Describe the morphology of the red blood cells.
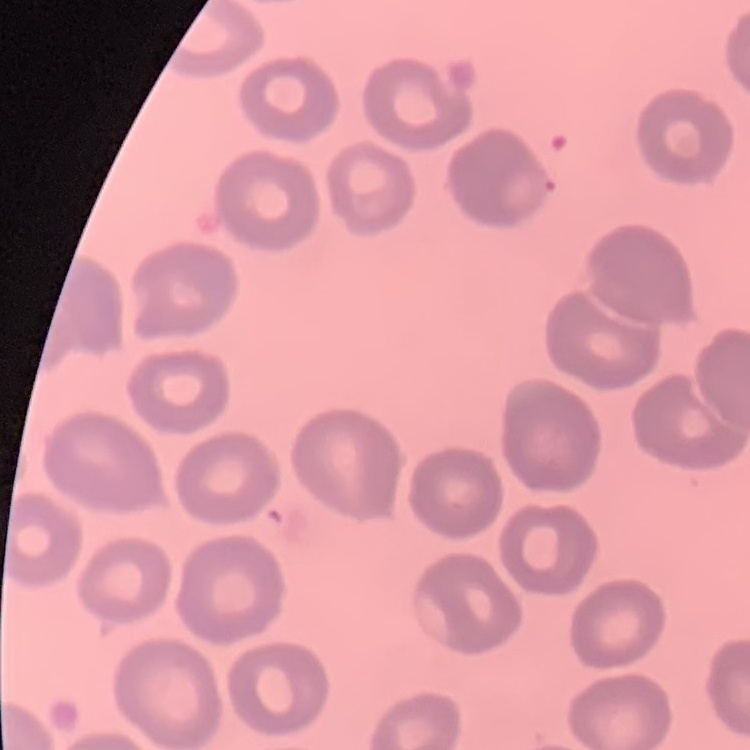
They show no rouleaux formation.

Stained with either Field's or Giemsa. Thin blood smear. One tile cut from a larger photomicrograph.